Locate and identify every blood parasite.
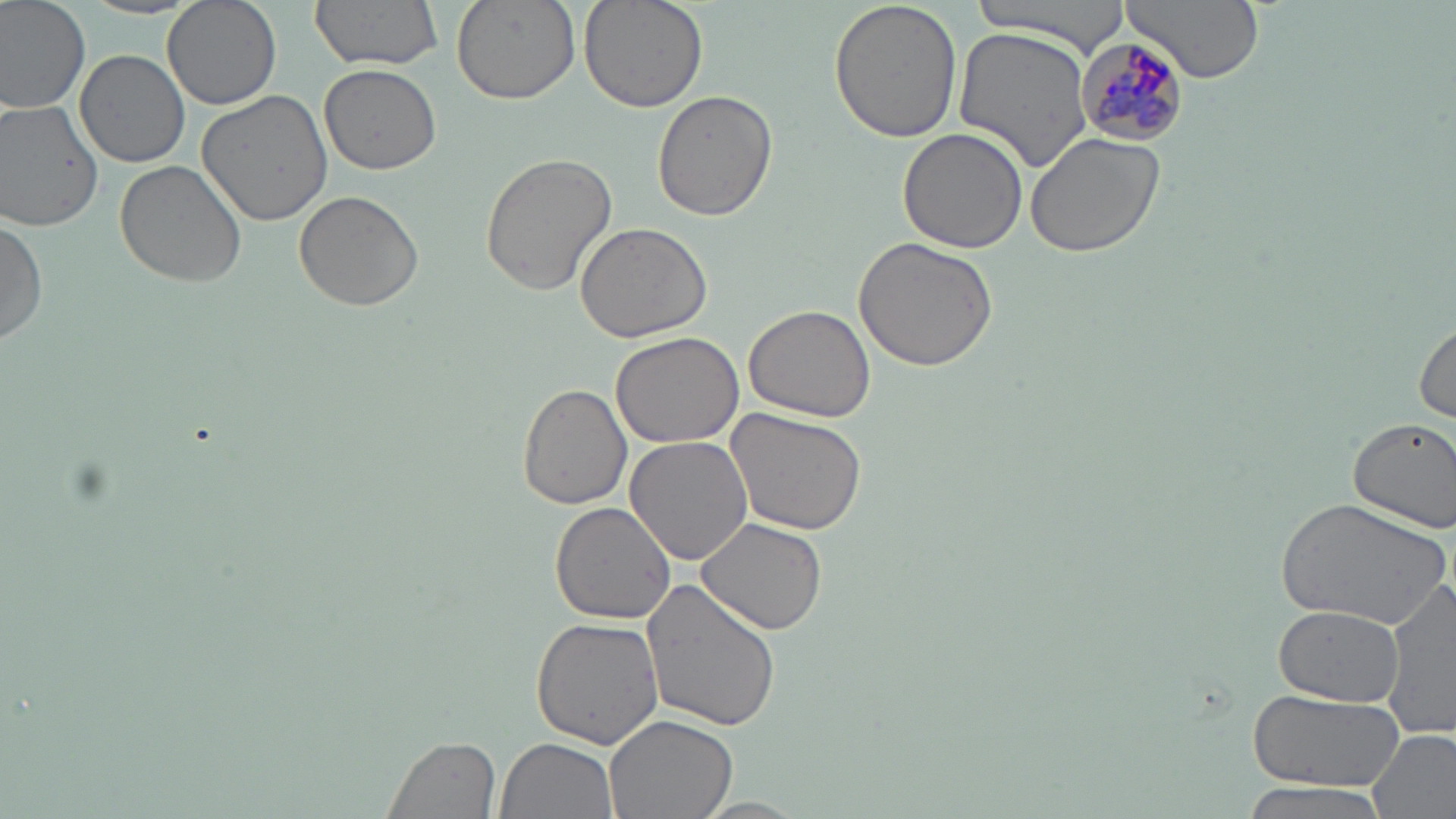

Approximate bounding boxes as (x1, y1, x2, y2) in pixels.
Plasmodium malariae-infected red blood cells: (1076, 36, 1190, 146).
No Plasmodium falciparum, Plasmodium ovale, Plasmodium vivax, Babesia divergens, or Trypanosoma brucei observed.

slide-level diagnosis = Plasmodium malariae
magnification = 1000x
image size = 1456×819 pixels
field of view = single
preparation = thin blood film
uninfected red blood cell locations = approximate bounding boxes as (x1, y1, x2, y2) in pixels: (0, 0, 90, 117), (163, 0, 282, 111), (309, 0, 444, 71), (449, 0, 579, 104), (577, 0, 708, 114), (829, 0, 963, 144), (969, 0, 1130, 53), (1122, 0, 1266, 85), (953, 25, 1095, 175), (77, 49, 189, 168), (321, 64, 440, 175), (195, 91, 335, 228), (653, 91, 778, 222), (0, 99, 104, 229), (899, 128, 1026, 252), (1026, 131, 1167, 258), (479, 152, 617, 296), (114, 160, 247, 288), (293, 190, 424, 313), (0, 213, 48, 346), (574, 222, 713, 344), (853, 237, 999, 373), (742, 304, 876, 422), (1414, 319, 1455, 423), (611, 331, 744, 448), (518, 383, 632, 511), (725, 407, 868, 535), (1348, 416, 1456, 531), (624, 436, 754, 567), (1274, 497, 1452, 628), (548, 502, 678, 625), (696, 518, 828, 636), (640, 578, 783, 735), (1381, 579, 1456, 739), (1273, 604, 1405, 707), (529, 616, 664, 750), (1244, 689, 1403, 793), (605, 714, 738, 819), (1367, 728, 1456, 819), (381, 735, 501, 819), (495, 738, 618, 819), (1239, 781, 1395, 818), (689, 798, 813, 818)
modality = light microscopy
stain = May-Grünwald-Giemsa